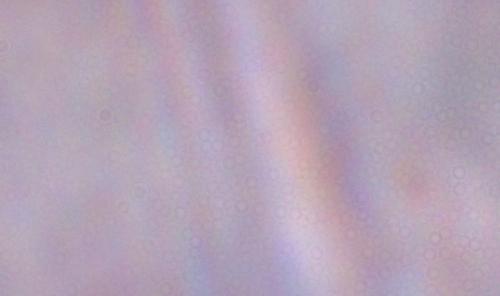

A trypanosome is shown. Photomicrograph. Captured at 1000x magnification.